Assess this cell for malaria.
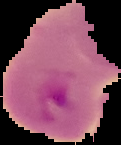

It is parasitized.

preparation: thin blood film
image_type: segmented cell region with the area outside set to black
image_size: 121×145 pixels